Comment on the morphology of the erythrocytes.
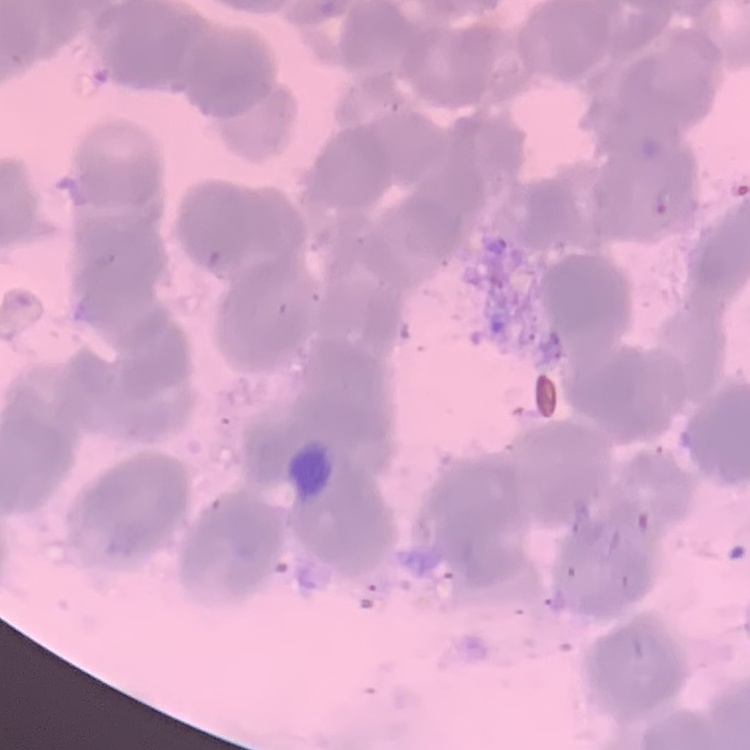
They show rouleaux formation.

Summary:
  - Preparation: thin blood smear
  - Image type: square crop of a larger photomicrograph
  - Stain: Field's or Giemsa